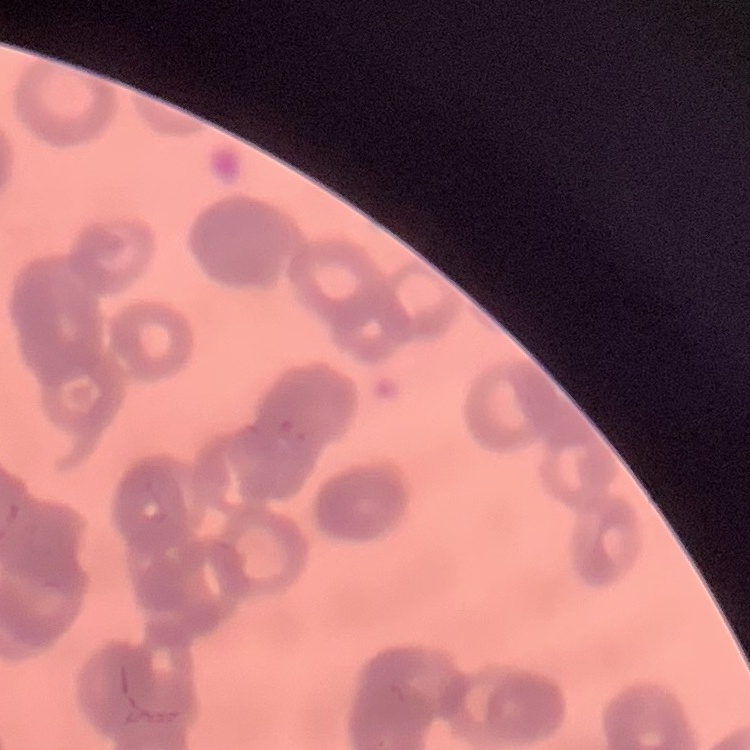

The red blood cells exhibit rouleaux formation. One tile cut from a larger photomicrograph. Thin blood smear. Stained with either Field's or Giemsa.